Report the malaria status of this cell.
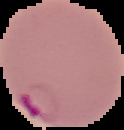
Parasitized.

image size = 124×130 pixels
preparation = thin blood smear
image type = segmented cell region on a black background